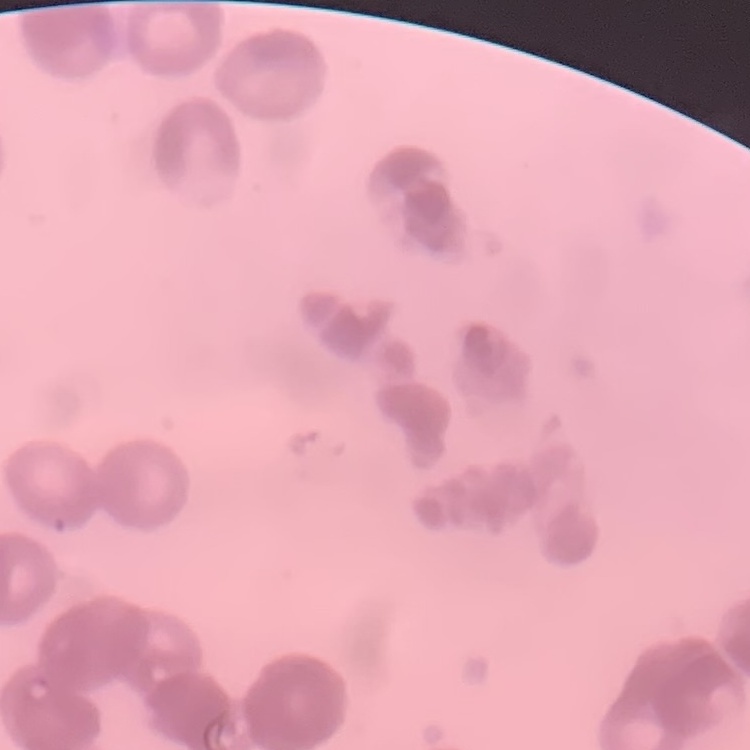

{
  "erythrocyte_morphology": "rouleaux formation",
  "preparation": "thin blood smear",
  "image_type": "one tile cut from a larger photomicrograph",
  "stain": "Field's or Giemsa"
}